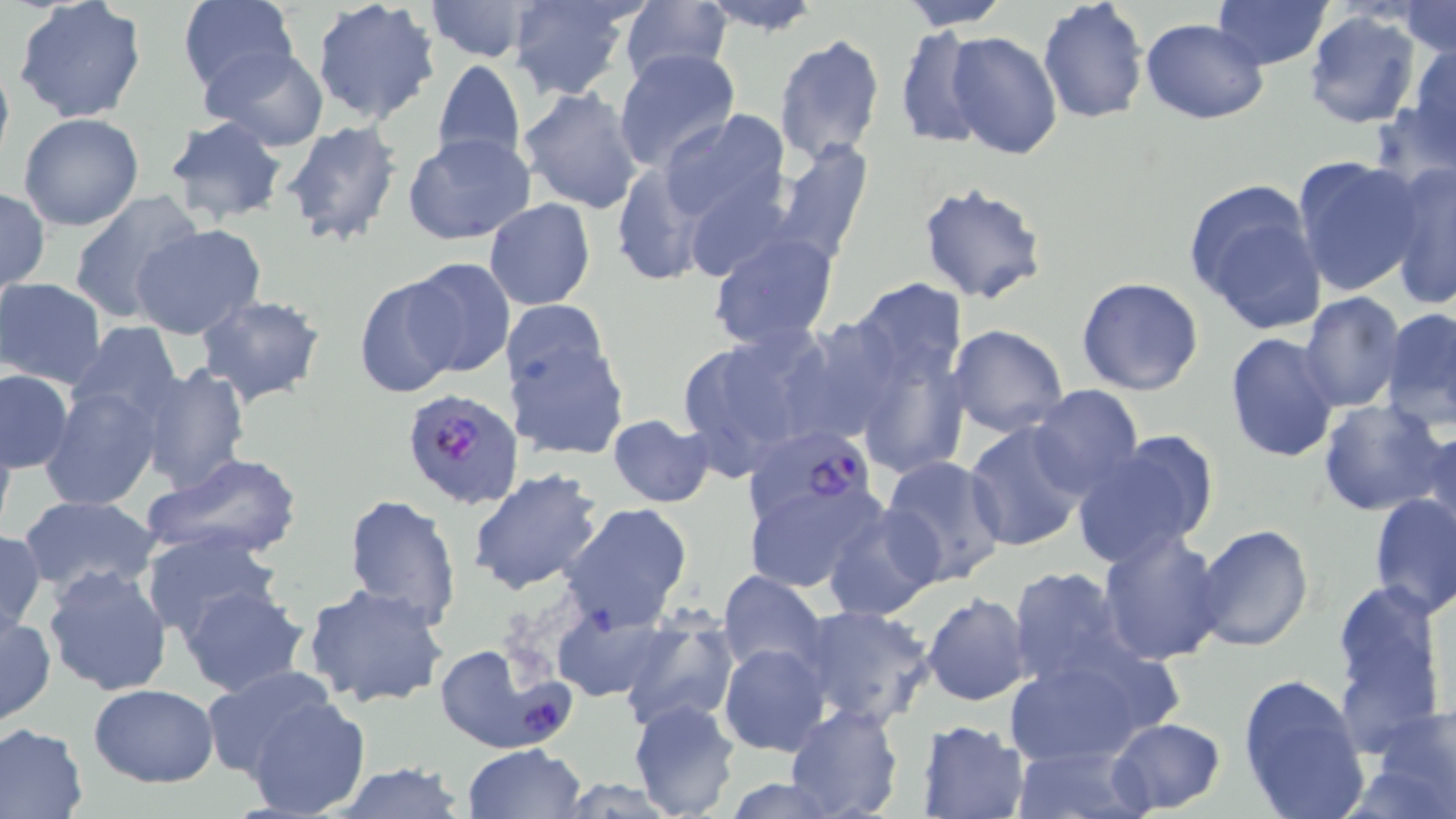

slide-level diagnosis = Plasmodium falciparum
magnification = 1000x
stain = May-Grünwald-Giemsa
field of view = one of a larger specimen
preparation = thin blood smear
Plasmodium falciparum-infected red blood cell locations = approximate bounding boxes as (x1,y1)-(x2,y2) corner pairs in pixels: (404,389)-(526,512), (749,420)-(877,539), (434,643)-(570,755)
uninfected red blood cell locations = approximate bounding boxes as (x1,y1)-(x2,y2) corner pairs in pixels: (176,0)-(298,96), (311,0)-(441,125), (422,0)-(543,63), (506,0)-(640,101), (697,0)-(823,34), (898,0)-(1011,30), (1036,0)-(1149,125), (1209,0)-(1333,70), (13,1)-(148,122), (618,2)-(732,85), (1397,3)-(1456,56), (1303,9)-(1423,129), (1141,18)-(1268,124), (892,27)-(991,150), (944,30)-(1066,160), (773,33)-(885,166), (1402,38)-(1455,164), (201,45)-(329,149), (613,48)-(740,174), (0,51)-(14,174), (432,58)-(525,169), (517,86)-(645,213), (657,109)-(792,233), (17,113)-(144,230), (163,117)-(289,226), (279,120)-(404,248), (402,132)-(534,246), (767,139)-(873,265), (1292,156)-(1426,297), (608,163)-(711,286), (1385,163)-(1455,308), (1185,180)-(1329,338), (917,181)-(1048,305), (0,186)-(49,297), (68,191)-(206,323), (485,199)-(595,311), (132,223)-(265,340), (707,232)-(839,351), (404,257)-(514,378), (353,274)-(467,400), (1076,276)-(1204,396), (851,278)-(966,387), (1,279)-(107,388), (1299,291)-(1405,412), (195,294)-(329,408), (829,298)-(973,481), (1382,306)-(1456,430), (66,322)-(184,428), (673,323)-(842,476), (947,323)-(1069,436), (507,325)-(629,464), (1223,332)-(1342,463), (138,362)-(250,494), (1,368)-(74,474), (40,384)-(163,511), (1029,384)-(1144,499), (1318,399)-(1449,518), (607,414)-(715,508), (963,422)-(1092,553), (1420,426)-(1456,541), (1071,431)-(1220,568), (146,453)-(303,564), (878,455)-(1008,587), (467,468)-(603,596), (739,471)-(884,594), (1369,493)-(1455,620), (342,494)-(462,630), (18,495)-(164,600), (561,501)-(692,631), (821,503)-(942,622), (1193,523)-(1314,650), (0,529)-(46,635), (142,530)-(281,642), (1097,530)-(1227,666), (41,563)-(173,696), (1007,566)-(1137,689), (718,571)-(829,678), (1331,580)-(1447,743), (302,582)-(447,709), (178,583)-(309,696), (921,593)-(1033,707), (796,603)-(935,731), (550,608)-(669,702), (0,610)-(54,726), (619,615)-(741,732), (718,643)-(831,756), (1001,653)-(1161,766), (201,666)-(342,781), (1237,672)-(1369,819), (89,683)-(219,785), (242,694)-(372,818), (627,700)-(743,819), (1362,703)-(1456,819), (785,704)-(905,819), (1107,717)-(1226,817), (915,720)-(1030,819), (0,722)-(90,817), (1010,741)-(1148,819), (463,744)-(585,819), (329,764)-(471,818), (716,777)-(853,816)
modality = optical microscopy
image size = 1456×819 pixels